Assess for malaria.
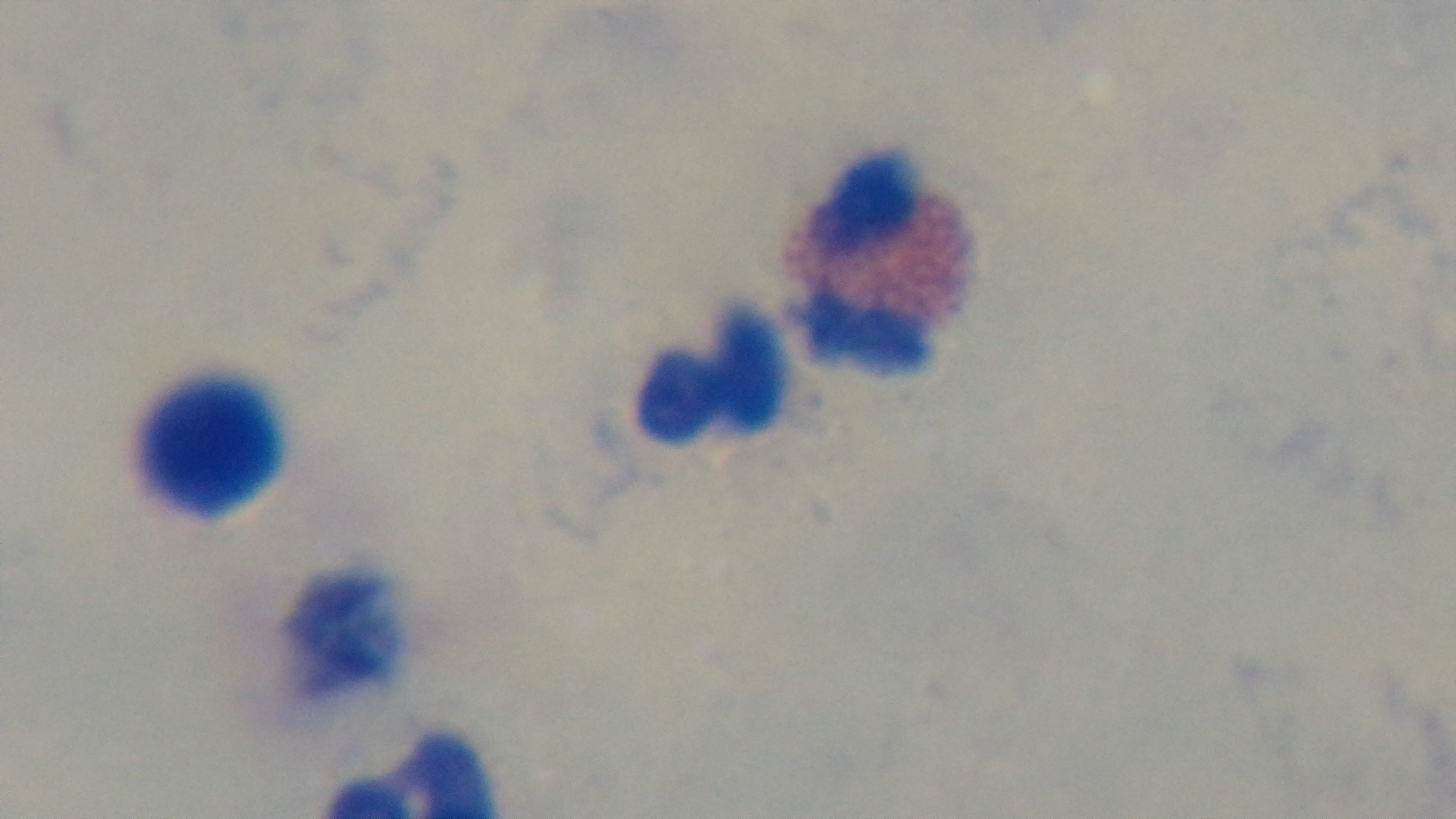
Negative.

Preparation: thick blood film. Light microscopy. Captured with a mounted 4K digital camera. Oil-immersion objective, 100x. Giemsa-stained. Single field of view.